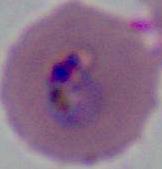
{
  "modality": "micrograph",
  "identification": "Plasmodium",
  "magnification": "400x or 1000x"
}